Classify this cell by malaria status.
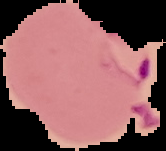

Parasitized.

Summary:
  - Image type: segmented cell region with the area outside set to black
  - Image size: 166×151 pixels
  - Preparation: thin blood smear